State which parasite is depicted.
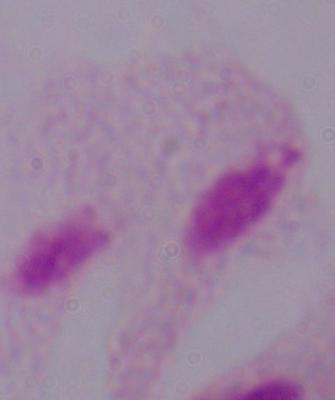

This is a trichomonad.

modality = micrograph
magnification = 1000x